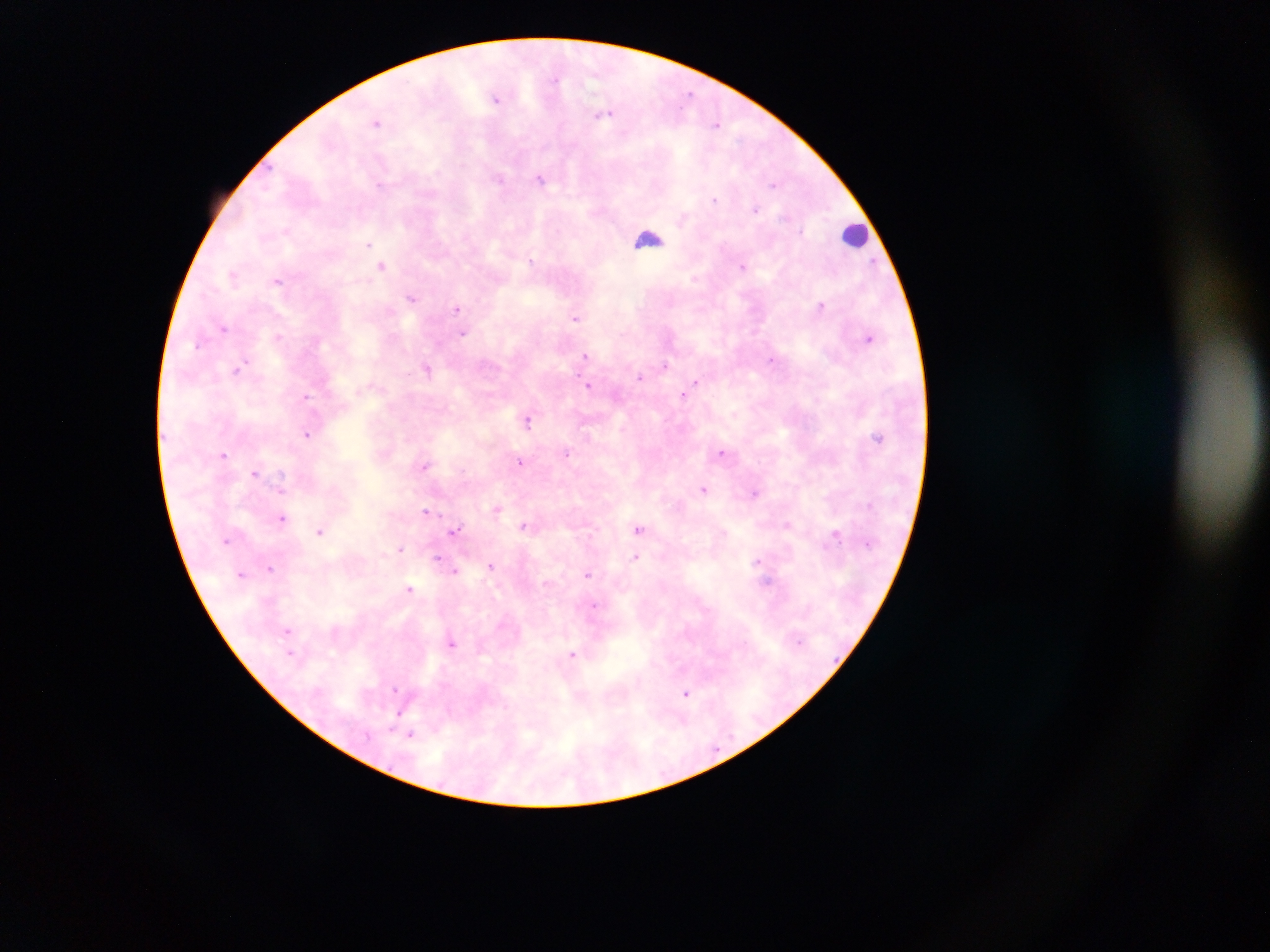
Approximate centers as (x, y) in pixels.
Summary:
  - Leukocyte locations: (856, 235), (646, 238)
  - Malaria parasite locations: (691, 92), (497, 100), (376, 122), (716, 122), (499, 179), (541, 180), (773, 184), (380, 185), (715, 199), (756, 209), (369, 242), (531, 261), (382, 265), (743, 266), (695, 278), (278, 281), (412, 297), (820, 306), (457, 309), (388, 313), (577, 319), (225, 326), (279, 334), (463, 334), (869, 335), (584, 356), (773, 360), (665, 366), (426, 369), (236, 371), (639, 376), (590, 385), (687, 395), (307, 397), (527, 420), (587, 433), (306, 434), (877, 437), (568, 452), (724, 452), (224, 455), (520, 462), (425, 465), (256, 472), (282, 476), (704, 487), (756, 495), (864, 504), (496, 508), (426, 510), (283, 519), (788, 525), (524, 527), (454, 529), (640, 529), (321, 530), (837, 532), (400, 549), (636, 558), (438, 559), (756, 560), (490, 565), (270, 567), (456, 572), (588, 575), (769, 582), (409, 588), (594, 604), (288, 629), (334, 629), (452, 643), (290, 652), (574, 654), (396, 688), (687, 692), (398, 712), (411, 736)
  - Image size: 1270×952 pixels
  - Preparation: thick blood smear
  - Country: Ghana
  - Field of view: single
  - Capture: mobile-phone photograph through a microscope